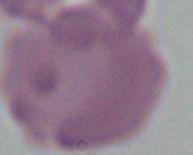

Photomicrograph. An erythrocyte is shown. Captured at 1000x magnification.